Identify the preparation type.
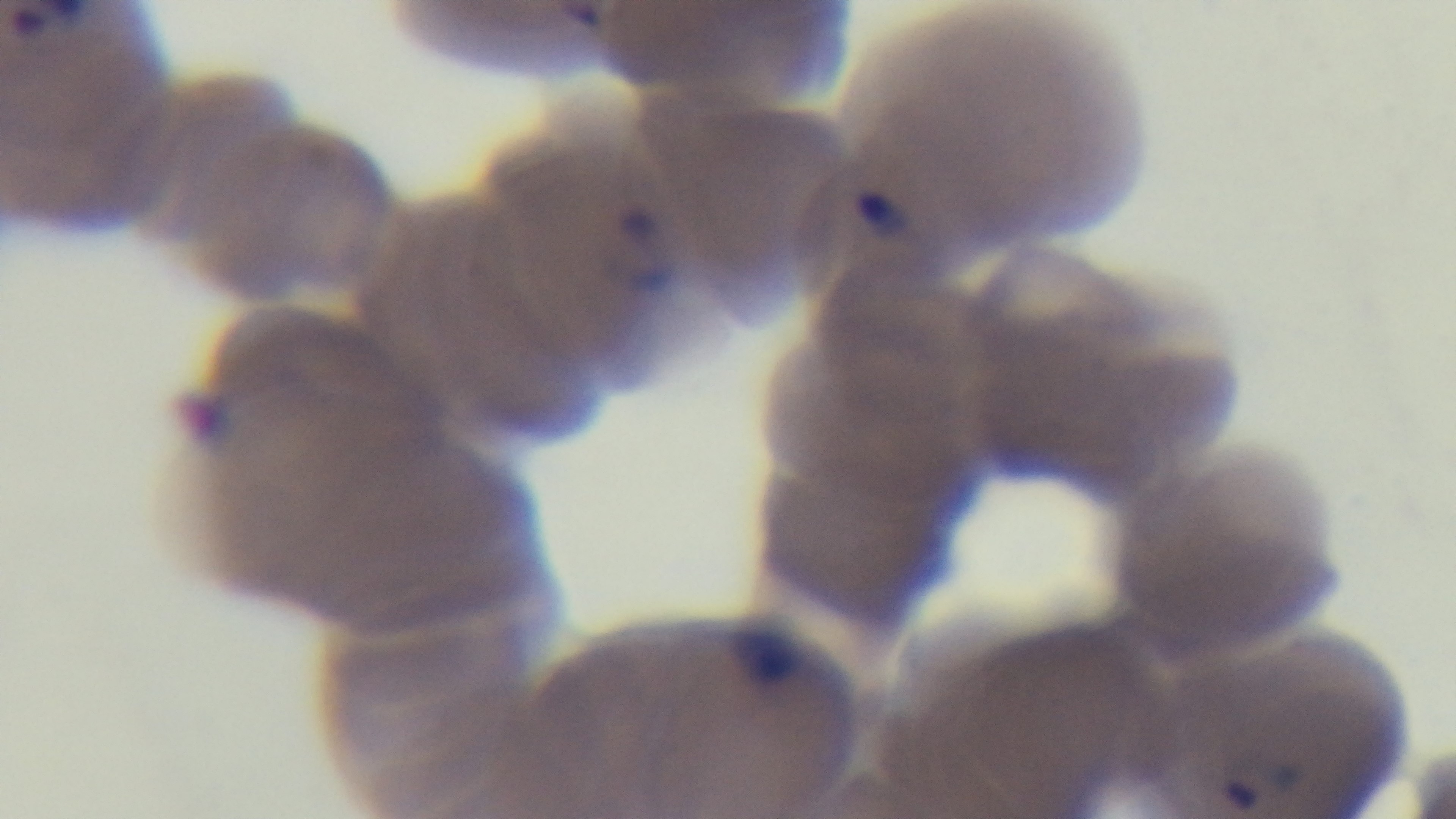

It is a thin blood film.

capture: mounted 4K digital camera
field_of_view: one from the slide
stain: Giemsa
objective: 100x oil immersion
malaria_status: positive
modality: light microscopy